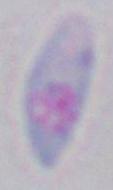

Summary:
  - Identification: Toxoplasma gondii
  - Modality: photomicrograph
  - Magnification: 1000x